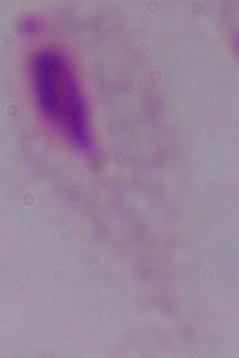
magnification = 1000x
identification = trichomonad
modality = micrograph